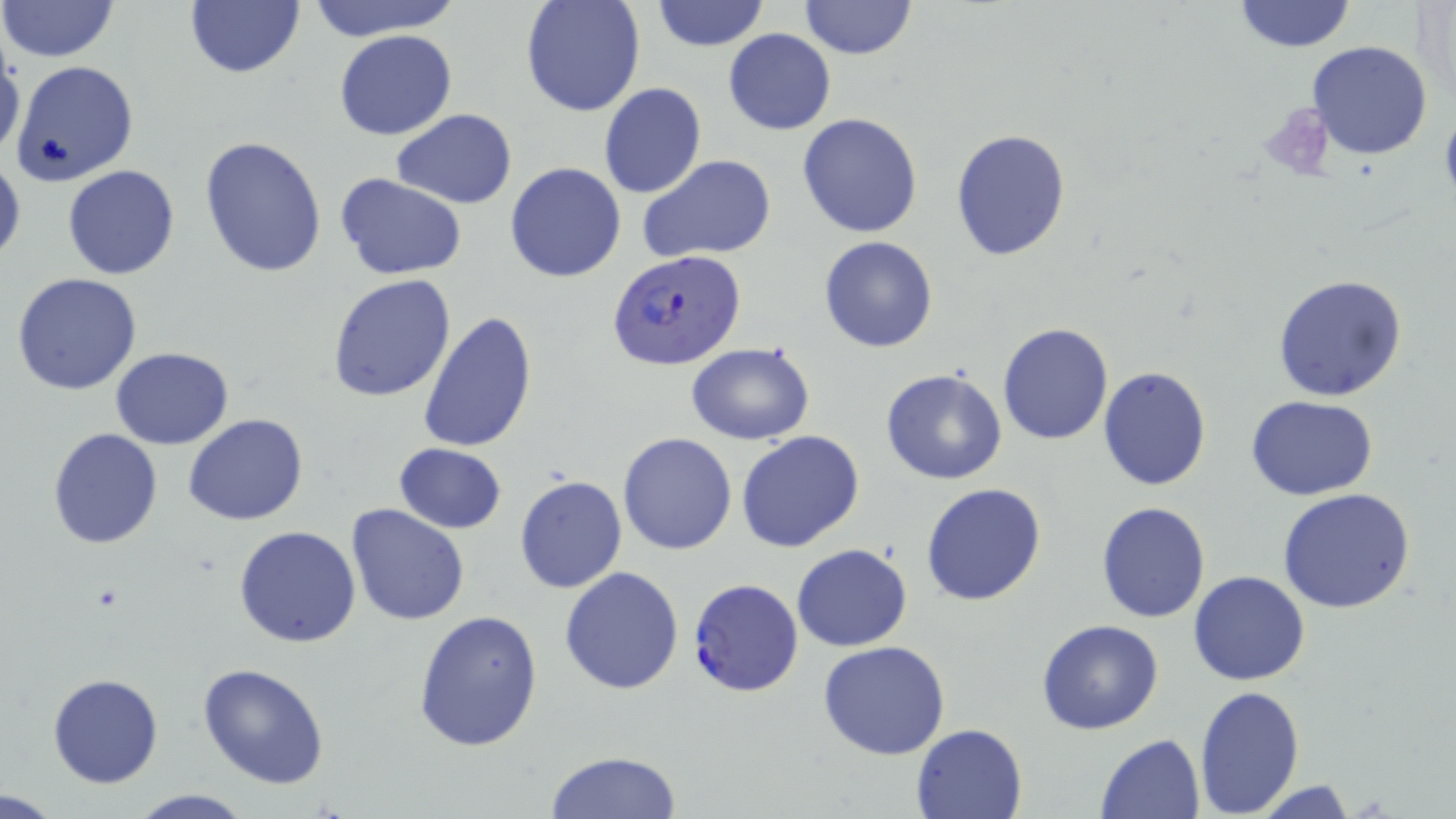
Summary:
  - Coordinate format: approximate bounding boxes as (x1, y1, x2, y2) in pixels
  - Plasmodium falciparum-infected red blood cell locations: (605, 252, 745, 374), (688, 577, 804, 697)
  - Platelet locations: (1262, 102, 1336, 179)
  - Uninfected red blood cell locations: (0, 0, 120, 65), (305, 0, 462, 42), (519, 0, 646, 118), (649, 0, 771, 51), (799, 0, 916, 59), (1229, 1, 1359, 52), (184, 2, 305, 79), (334, 29, 457, 141), (722, 29, 836, 135), (0, 38, 26, 163), (1307, 39, 1433, 160), (12, 60, 139, 185), (599, 83, 707, 198), (391, 108, 516, 208), (797, 113, 923, 238), (951, 128, 1072, 262), (200, 135, 328, 277), (638, 155, 776, 261), (0, 157, 24, 267), (504, 162, 628, 283), (62, 165, 180, 279), (334, 172, 468, 279), (818, 235, 939, 353), (12, 272, 143, 395), (328, 274, 457, 401), (1270, 274, 1408, 402), (418, 308, 538, 453), (997, 320, 1112, 445), (684, 342, 815, 446), (110, 346, 234, 449), (1098, 365, 1212, 492), (880, 367, 1007, 486), (1246, 394, 1378, 500), (185, 413, 309, 526), (47, 428, 162, 548), (736, 431, 865, 554), (617, 432, 739, 555), (392, 443, 507, 533), (514, 474, 625, 594), (920, 482, 1047, 607), (1277, 489, 1419, 614), (1095, 501, 1211, 623), (345, 503, 471, 626), (234, 525, 362, 648), (791, 543, 912, 651), (559, 566, 685, 696), (1188, 570, 1310, 687), (413, 608, 544, 753), (1035, 619, 1165, 734), (817, 639, 951, 760), (198, 663, 330, 788), (46, 674, 163, 789), (1193, 684, 1304, 815), (912, 723, 1026, 818), (1096, 733, 1205, 817), (543, 750, 682, 818), (1245, 779, 1363, 817), (0, 789, 67, 818), (124, 790, 258, 817)
  - Slide-level diagnosis: Plasmodium falciparum
  - Stain: May-Grünwald-Giemsa
  - Preparation: thin blood smear
  - Magnification: 1000x
  - Modality: light microscopy
  - Image size: 1456×819 pixels
  - Field of view: single